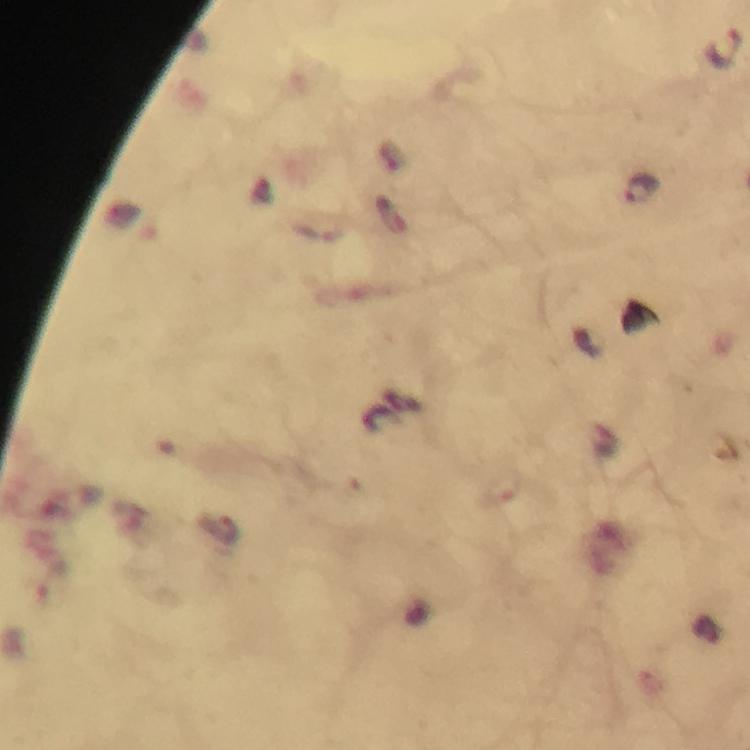

Approximate centers as (x, y) in pixels. Malaria parasite locations: (725, 46), (642, 189). Thick smear. Image is 750×750 pixels. Photographed with a smartphone mounted on the microscope. Giemsa-stained preparation. From a diagnostic examination for malaria. Immersion oil applied. At 100x magnification. A crop from one field of view.